Locate and identify every blood parasite.
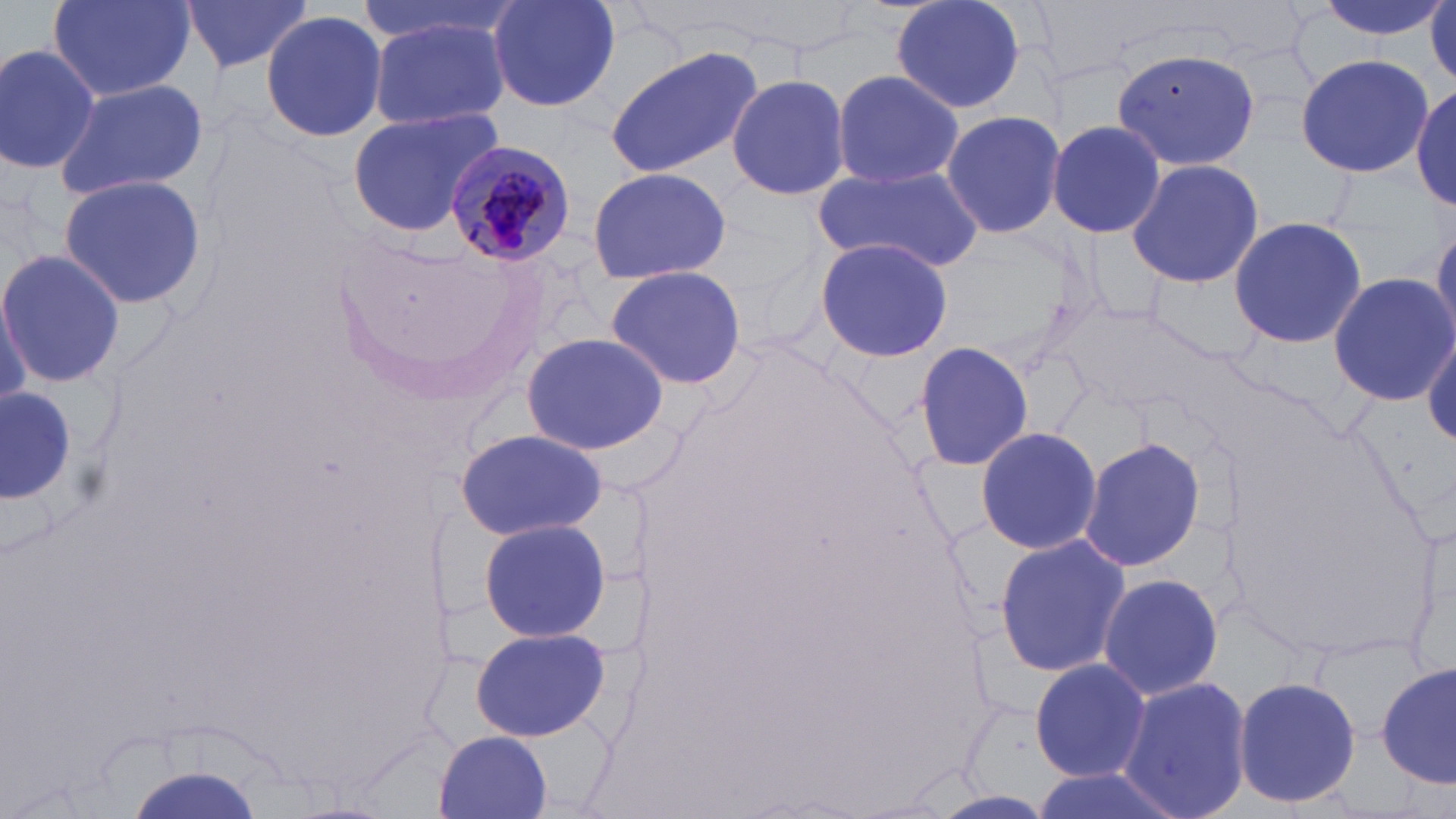
Approximate bounding boxes as named x1/y1/x2/y2 corners in pixels.
Plasmodium malariae-infected red blood cells: (x1=444, y1=138, x2=574, y2=267).
No Plasmodium falciparum, Plasmodium ovale, Plasmodium vivax, Babesia divergens, or Trypanosoma brucei observed.

Summary:
  - Uninfected red blood cell locations: (x1=182, y1=0, x2=312, y2=77), (x1=354, y1=0, x2=514, y2=48), (x1=482, y1=0, x2=624, y2=112), (x1=887, y1=0, x2=1028, y2=116), (x1=1304, y1=0, x2=1449, y2=43), (x1=49, y1=1, x2=194, y2=101), (x1=259, y1=10, x2=388, y2=141), (x1=367, y1=13, x2=511, y2=131), (x1=0, y1=42, x2=99, y2=176), (x1=605, y1=47, x2=764, y2=177), (x1=1110, y1=48, x2=1262, y2=171), (x1=1296, y1=54, x2=1432, y2=176), (x1=832, y1=68, x2=963, y2=191), (x1=726, y1=73, x2=850, y2=201), (x1=53, y1=78, x2=208, y2=201), (x1=1413, y1=85, x2=1454, y2=209), (x1=346, y1=106, x2=508, y2=237), (x1=941, y1=109, x2=1065, y2=241), (x1=1046, y1=119, x2=1168, y2=240), (x1=1124, y1=157, x2=1264, y2=288), (x1=586, y1=166, x2=731, y2=283), (x1=814, y1=170, x2=979, y2=270), (x1=56, y1=174, x2=208, y2=313), (x1=1228, y1=216, x2=1367, y2=351), (x1=1430, y1=222, x2=1456, y2=340), (x1=814, y1=237, x2=953, y2=362), (x1=0, y1=247, x2=125, y2=390), (x1=603, y1=264, x2=748, y2=391), (x1=1328, y1=272, x2=1455, y2=405), (x1=1146, y1=273, x2=1268, y2=363), (x1=1053, y1=306, x2=1219, y2=418), (x1=1422, y1=331, x2=1456, y2=445), (x1=520, y1=332, x2=669, y2=456), (x1=913, y1=340, x2=1034, y2=470), (x1=0, y1=386, x2=78, y2=508), (x1=973, y1=423, x2=1102, y2=557), (x1=455, y1=428, x2=607, y2=540), (x1=1078, y1=436, x2=1206, y2=575), (x1=478, y1=516, x2=611, y2=644), (x1=993, y1=532, x2=1132, y2=680), (x1=1095, y1=570, x2=1225, y2=703), (x1=469, y1=624, x2=610, y2=743), (x1=1029, y1=657, x2=1150, y2=782), (x1=1379, y1=662, x2=1455, y2=790), (x1=1233, y1=674, x2=1361, y2=812), (x1=1118, y1=675, x2=1252, y2=819), (x1=435, y1=731, x2=552, y2=817), (x1=1025, y1=768, x2=1174, y2=819)
  - Slide-level diagnosis: Plasmodium malariae
  - Image size: 1456×819 pixels
  - Preparation: thin blood film
  - Modality: optical microscopy
  - Magnification: 1000x
  - Stain: May-Grünwald-Giemsa
  - Field of view: single